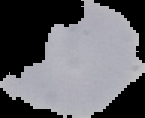 Image is 145×118 pixels. From a thin blood smear. Segmented cell region on a black background. Malaria status: uninfected.